Describe the morphology of the red blood cells.
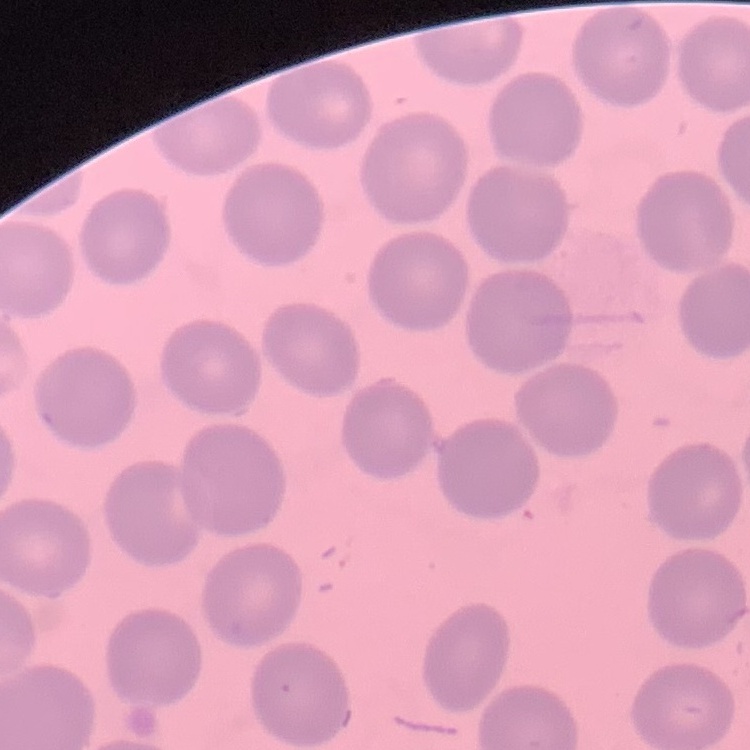

No rouleaux formation.

One tile cut from a larger photomicrograph. Stained with either Field's or Giemsa. Thin blood film.